Locate every blood parasite and identify its species.
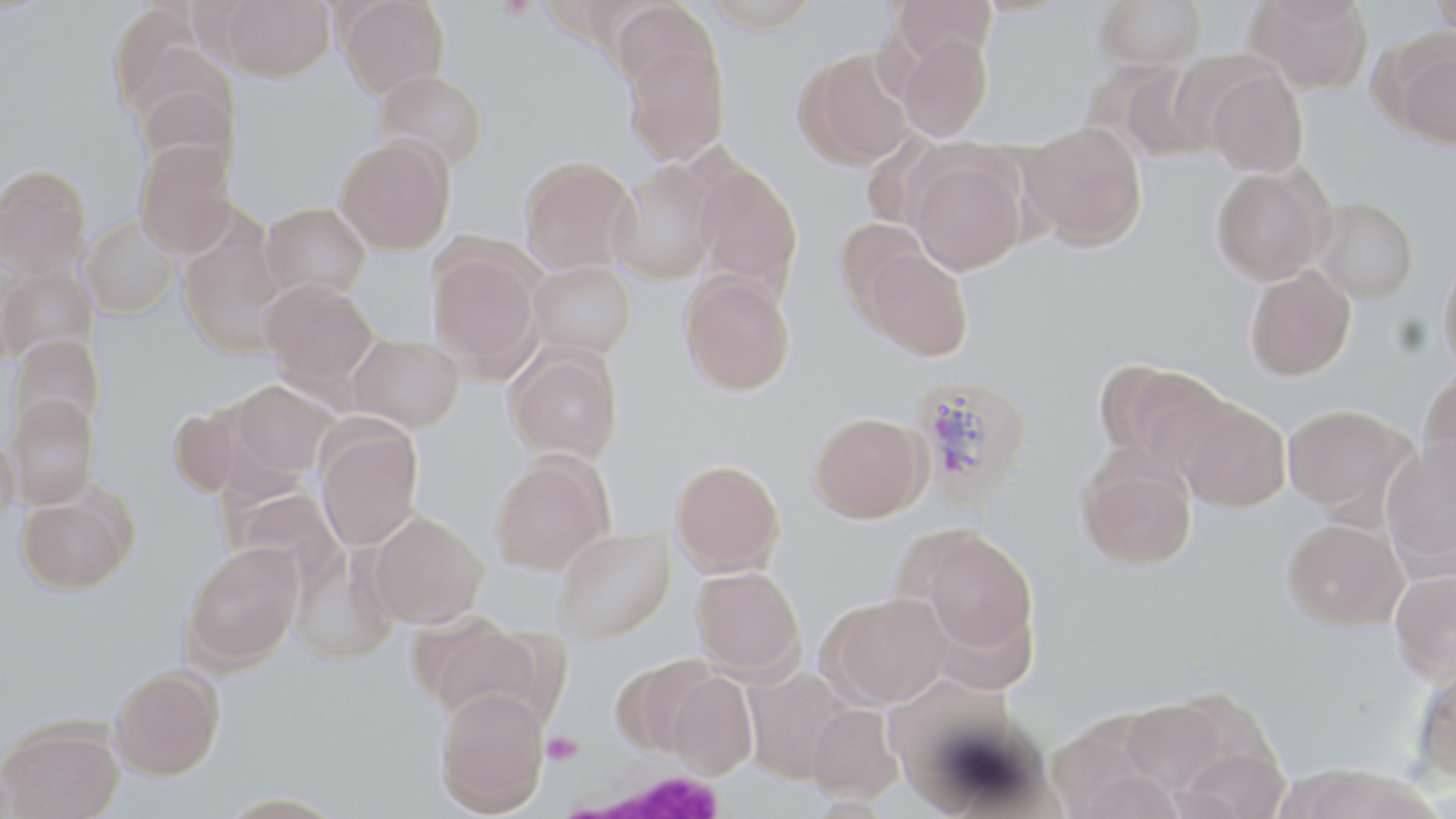

Approximate bounding boxes as (x1,y1)-(x2,y2) corner pairs in pixels.
Plasmodium vivax-infected red blood cells: (911,375)-(1034,507).
No Plasmodium falciparum, Plasmodium ovale, Plasmodium malariae, Babesia divergens, or Trypanosoma brucei observed.

Summary:
  - White blood cell locations: (564,763)-(737,818)
  - Platelet locations: (496,0)-(537,21), (543,732)-(582,765)
  - Uninfected red blood cell locations: (219,0)-(334,81), (336,0)-(450,99), (703,0)-(819,32), (890,0)-(996,65), (1095,0)-(1207,70), (1244,0)-(1373,96), (1428,0)-(1456,38), (610,1)-(720,94), (107,3)-(225,127), (897,30)-(992,141), (1386,37)-(1456,150), (622,40)-(730,165), (796,49)-(913,168), (1094,62)-(1212,162), (1205,67)-(1308,177), (373,69)-(489,173), (135,82)-(239,182), (1019,121)-(1149,250), (334,135)-(455,254), (134,141)-(238,258), (909,155)-(1027,275), (519,156)-(638,274), (610,160)-(724,285), (692,162)-(803,296), (0,164)-(93,280), (1211,166)-(1331,284), (1313,198)-(1418,304), (261,202)-(370,301), (80,215)-(179,319), (834,218)-(930,316), (177,233)-(291,358), (860,249)-(973,361), (428,250)-(541,376), (1437,253)-(1456,377), (527,260)-(636,360), (0,264)-(99,365), (1244,265)-(1356,380), (679,271)-(796,396), (261,279)-(379,390), (347,333)-(464,432), (8,334)-(105,435), (506,347)-(623,466), (1096,359)-(1228,471), (1417,369)-(1456,483), (229,380)-(338,478), (4,393)-(100,509), (1174,396)-(1291,512), (1283,404)-(1411,515), (168,405)-(250,500), (809,411)-(930,523), (315,422)-(423,550), (0,427)-(19,531), (1380,440)-(1456,572), (490,452)-(614,575), (1077,457)-(1197,570), (671,458)-(786,577), (15,493)-(134,594), (369,510)-(488,628), (1281,517)-(1408,631), (553,528)-(675,643), (917,530)-(1039,661), (182,543)-(303,670), (290,545)-(398,664), (691,565)-(805,678), (1390,567)-(1456,683), (823,592)-(952,708), (420,616)-(544,725), (611,654)-(717,759), (1413,660)-(1456,786), (109,665)-(226,779), (743,668)-(855,784), (664,671)-(759,779), (434,686)-(551,815), (1118,697)-(1230,796), (806,703)-(902,803), (0,720)-(124,818), (1045,722)-(1167,817), (1173,744)-(1291,819)
  - Slide-level diagnosis: Plasmodium vivax
  - Modality: optical microscopy
  - Preparation: thin blood film
  - Field of view: one of a larger specimen
  - Stain: May-Grünwald-Giemsa
  - Magnification: 1000x
  - Image size: 1456×819 pixels